Report the malaria status of this cell.
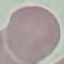
It is uninfected.

Summary:
  - Capture: smartphone camera at the microscope eyepiece
  - Preparation: thin blood film
  - Stain: Giemsa
  - Image type: cell patch, automatically extracted from a larger field of view and resized to 64 × 64 pixels